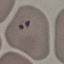
malaria status = parasitized
stain = Giemsa
image type = automatically extracted cell patch, resized to 64 × 64 pixels
preparation = thin blood film
capture = smartphone camera at the microscope eyepiece